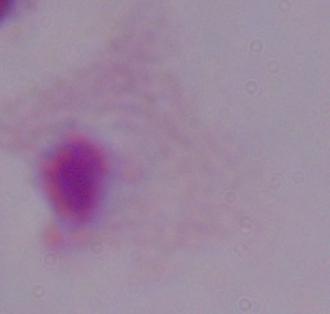

Summary:
  - Identification: trichomonad
  - Magnification: 1000x
  - Modality: micrograph